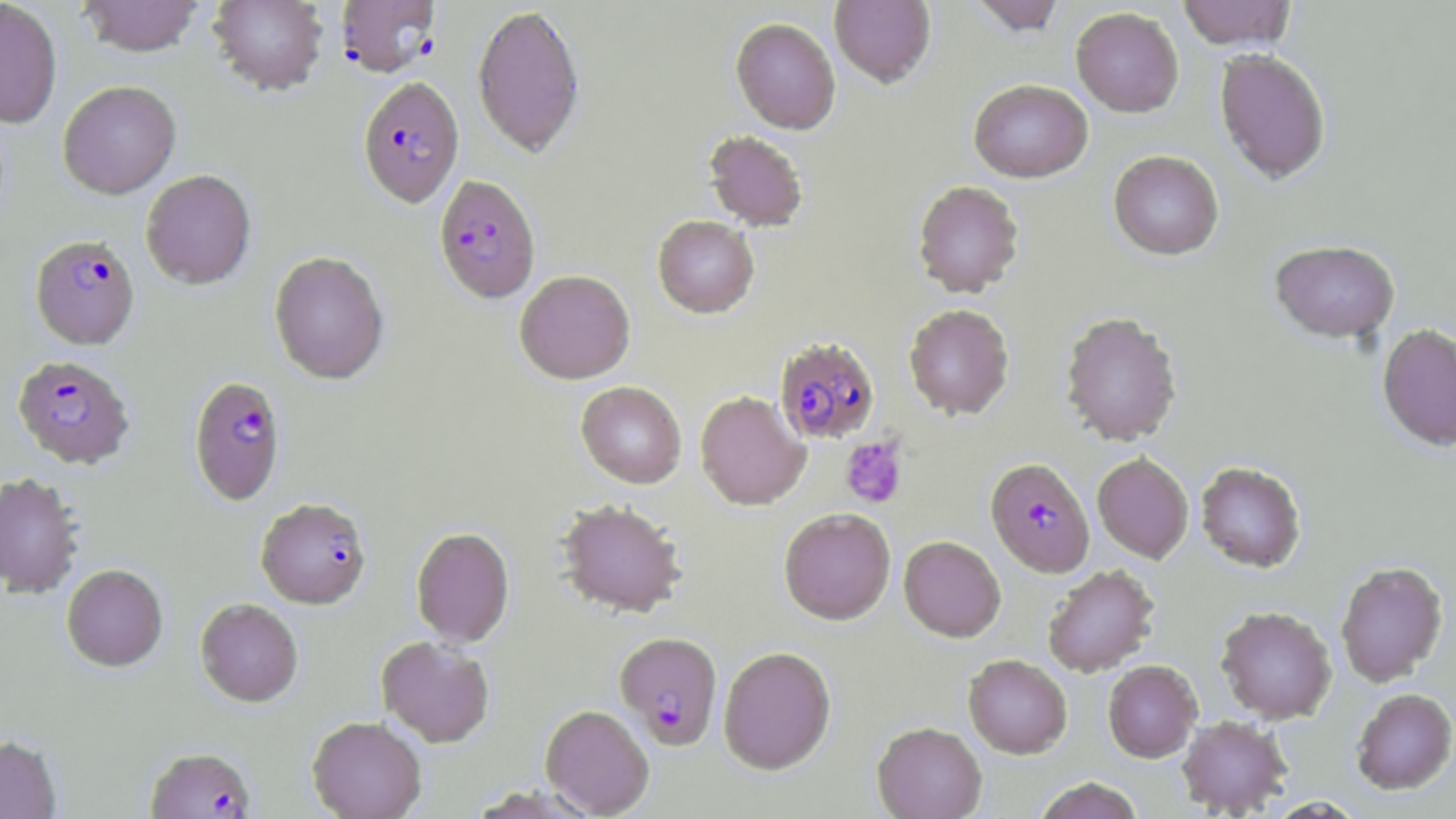
slide-level diagnosis = Plasmodium falciparum
image size = 1456×819 pixels
Plasmodium falciparum-infected red blood cell locations = approximate bounding boxes as [x1, y1, x2, y2] in pixels: [336, 0, 441, 77], [357, 76, 464, 208], [433, 175, 541, 305], [30, 234, 140, 349], [775, 337, 880, 444], [13, 355, 135, 469], [188, 376, 286, 505], [985, 457, 1095, 577], [256, 498, 372, 610], [614, 632, 723, 749], [145, 747, 256, 818]
stain = May-Grünwald-Giemsa
uninfected red blood cell locations = approximate bounding boxes as [x1, y1, x2, y2] in pixels: [0, 0, 62, 128], [77, 0, 205, 58], [208, 0, 329, 96], [829, 0, 936, 88], [968, 0, 1067, 35], [1177, 0, 1297, 51], [472, 4, 585, 158], [1070, 6, 1184, 117], [730, 17, 841, 134], [1214, 48, 1331, 185], [968, 79, 1093, 182], [58, 81, 181, 199], [704, 129, 808, 231], [1108, 149, 1224, 260], [140, 170, 256, 290], [912, 179, 1025, 298], [652, 216, 760, 319], [1269, 239, 1400, 343], [269, 251, 389, 384], [514, 270, 635, 384], [903, 303, 1014, 420], [1059, 310, 1183, 446], [1377, 324, 1456, 451], [576, 381, 686, 488], [695, 390, 810, 511], [1092, 452, 1194, 563], [1195, 461, 1307, 573], [0, 472, 84, 599], [556, 499, 686, 619], [778, 507, 896, 625], [411, 527, 514, 647], [899, 536, 1006, 641], [1335, 560, 1449, 687], [62, 564, 168, 672], [1042, 564, 1159, 677], [195, 598, 303, 707], [1216, 605, 1337, 723], [376, 636, 495, 748], [718, 646, 836, 774], [963, 654, 1072, 758], [1103, 660, 1202, 762], [1351, 688, 1456, 794], [540, 704, 654, 817], [1177, 715, 1292, 816], [307, 716, 427, 819], [872, 721, 987, 819], [0, 734, 62, 819], [1033, 777, 1143, 819]
modality = light microscopy
magnification = 1000x
platelet locations = approximate bounding boxes as [x1, y1, x2, y2] in pixels: [840, 436, 907, 508]
preparation = thin blood smear
field of view = single